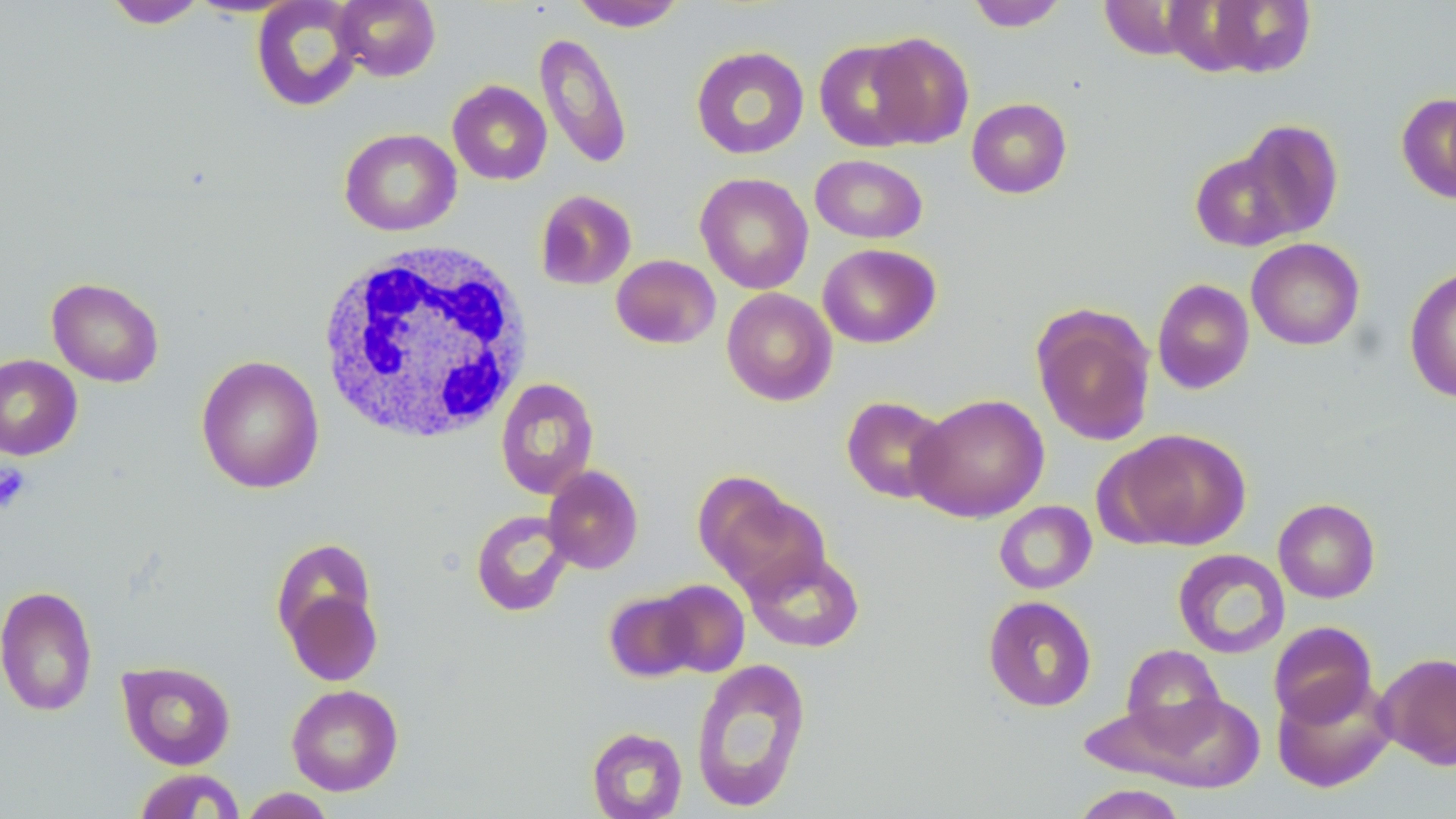 Approximate bounding boxes as named x1/y1/x2/y2 corners in pixels. Uninfected red blood cell locations: (x1=103, y1=0, x2=208, y2=29), (x1=251, y1=0, x2=364, y2=112), (x1=334, y1=0, x2=440, y2=81), (x1=569, y1=0, x2=686, y2=31), (x1=965, y1=0, x2=1068, y2=31), (x1=1197, y1=1, x2=1317, y2=78), (x1=865, y1=31, x2=974, y2=148), (x1=534, y1=32, x2=633, y2=171), (x1=814, y1=39, x2=927, y2=152), (x1=691, y1=46, x2=809, y2=159), (x1=448, y1=80, x2=552, y2=185), (x1=1396, y1=91, x2=1456, y2=204), (x1=966, y1=97, x2=1072, y2=198), (x1=1236, y1=119, x2=1344, y2=240), (x1=339, y1=128, x2=462, y2=236), (x1=1190, y1=151, x2=1296, y2=251), (x1=810, y1=154, x2=927, y2=244), (x1=695, y1=172, x2=813, y2=294), (x1=534, y1=189, x2=637, y2=290), (x1=1246, y1=238, x2=1365, y2=351), (x1=818, y1=243, x2=941, y2=348), (x1=611, y1=254, x2=721, y2=349), (x1=1404, y1=265, x2=1456, y2=403), (x1=47, y1=277, x2=164, y2=387), (x1=1152, y1=278, x2=1254, y2=394), (x1=721, y1=287, x2=837, y2=406), (x1=1031, y1=304, x2=1156, y2=446), (x1=0, y1=354, x2=83, y2=460), (x1=196, y1=356, x2=324, y2=494), (x1=496, y1=378, x2=599, y2=498), (x1=908, y1=393, x2=1050, y2=523), (x1=841, y1=396, x2=951, y2=504), (x1=1105, y1=428, x2=1253, y2=551), (x1=542, y1=466, x2=643, y2=574), (x1=694, y1=474, x2=831, y2=598), (x1=1273, y1=498, x2=1380, y2=603), (x1=994, y1=500, x2=1097, y2=594), (x1=471, y1=509, x2=574, y2=617), (x1=271, y1=537, x2=379, y2=652), (x1=744, y1=548, x2=865, y2=653), (x1=1173, y1=548, x2=1291, y2=659), (x1=653, y1=579, x2=750, y2=677), (x1=280, y1=581, x2=384, y2=688), (x1=0, y1=585, x2=98, y2=717), (x1=604, y1=590, x2=702, y2=682), (x1=983, y1=595, x2=1097, y2=712), (x1=1268, y1=621, x2=1378, y2=727), (x1=1121, y1=644, x2=1226, y2=742), (x1=1375, y1=651, x2=1456, y2=770), (x1=690, y1=658, x2=812, y2=811), (x1=118, y1=660, x2=236, y2=770), (x1=1272, y1=676, x2=1396, y2=793), (x1=286, y1=684, x2=403, y2=796), (x1=1108, y1=693, x2=1266, y2=791), (x1=587, y1=727, x2=688, y2=819), (x1=132, y1=768, x2=246, y2=818), (x1=1070, y1=784, x2=1187, y2=819), (x1=238, y1=788, x2=337, y2=818). White blood cell locations: (x1=313, y1=241, x2=535, y2=447). Platelet locations: (x1=0, y1=463, x2=33, y2=513). Slide-level diagnosis: negative for blood parasites. May-Grünwald-Giemsa stain. One field of a larger specimen. Thin blood film. Image is 1456×819 pixels. Captured at 1000x magnification. Optical microscopy.